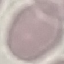
Summary:
  - Result: no malaria parasites detected
  - Preparation: thin blood smear
  - Image type: cell patch, automatically extracted from a larger field of view and resized to 64 × 64 pixels
  - Stain: Giemsa
  - Capture: smartphone camera at the microscope eyepiece